Give the preparation type.
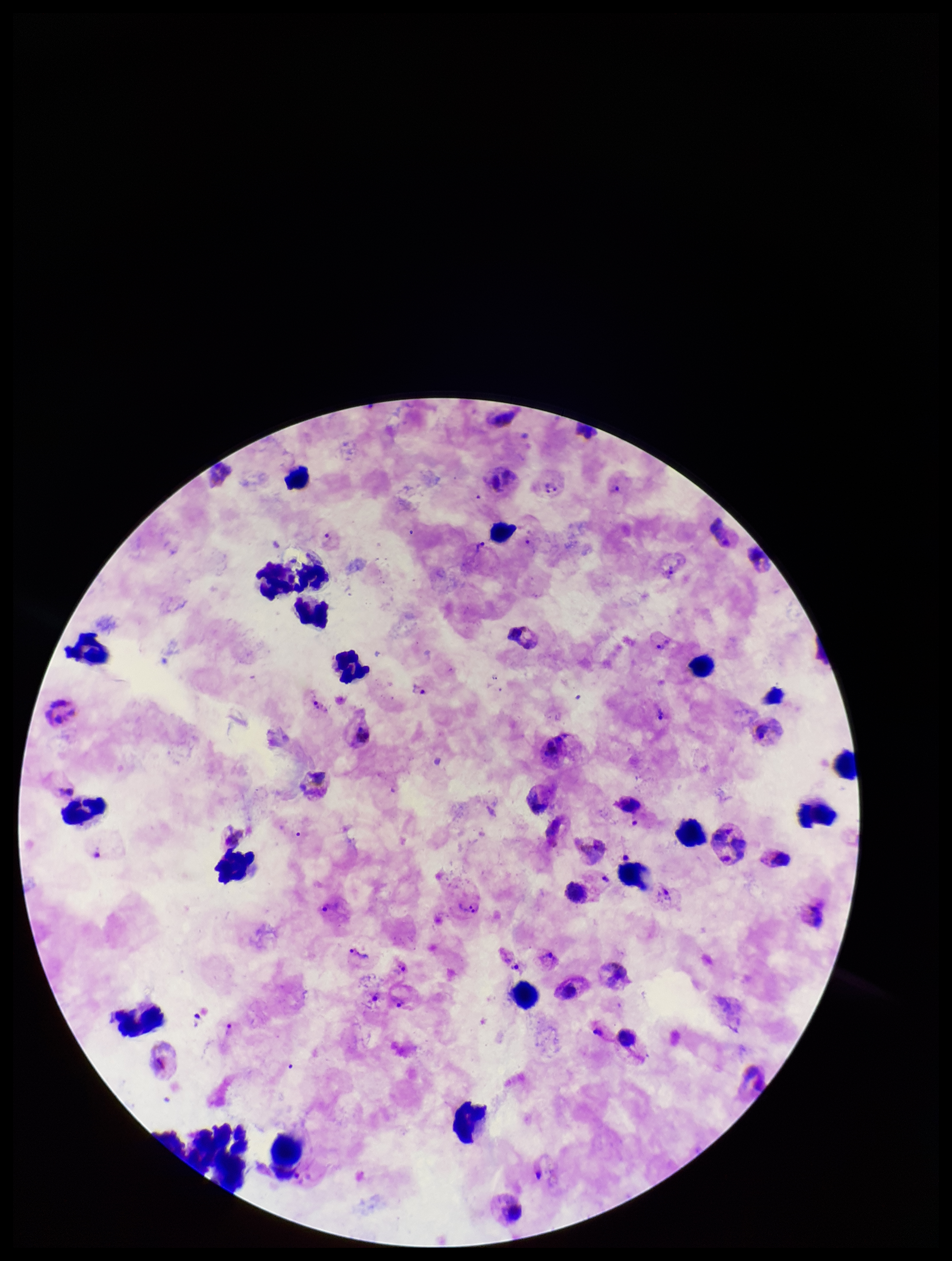

It is a thick blood smear.

Summary:
  - Field of view: single
  - Image size: 952×1261 pixels
  - Capture: smartphone photograph through the microscope eyepiece
  - Leukocyte count: 39
  - Plasmodium parasites: detected
  - Species reported for this patient: Plasmodium vivax
  - Stain: Giemsa
  - Patient malaria status: infected
  - Parasite count: 13